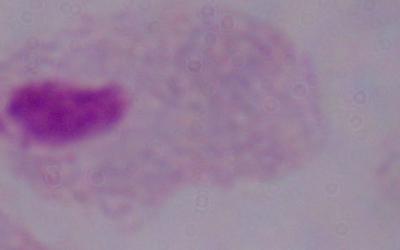

Summary:
  - Identification: trichomonad
  - Magnification: 1000x
  - Modality: photomicrograph